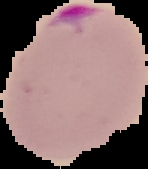

The area outside the segmented cell region is set to black. Image is 148×169 pixels. Result: malaria parasites identified. From a thin blood smear.